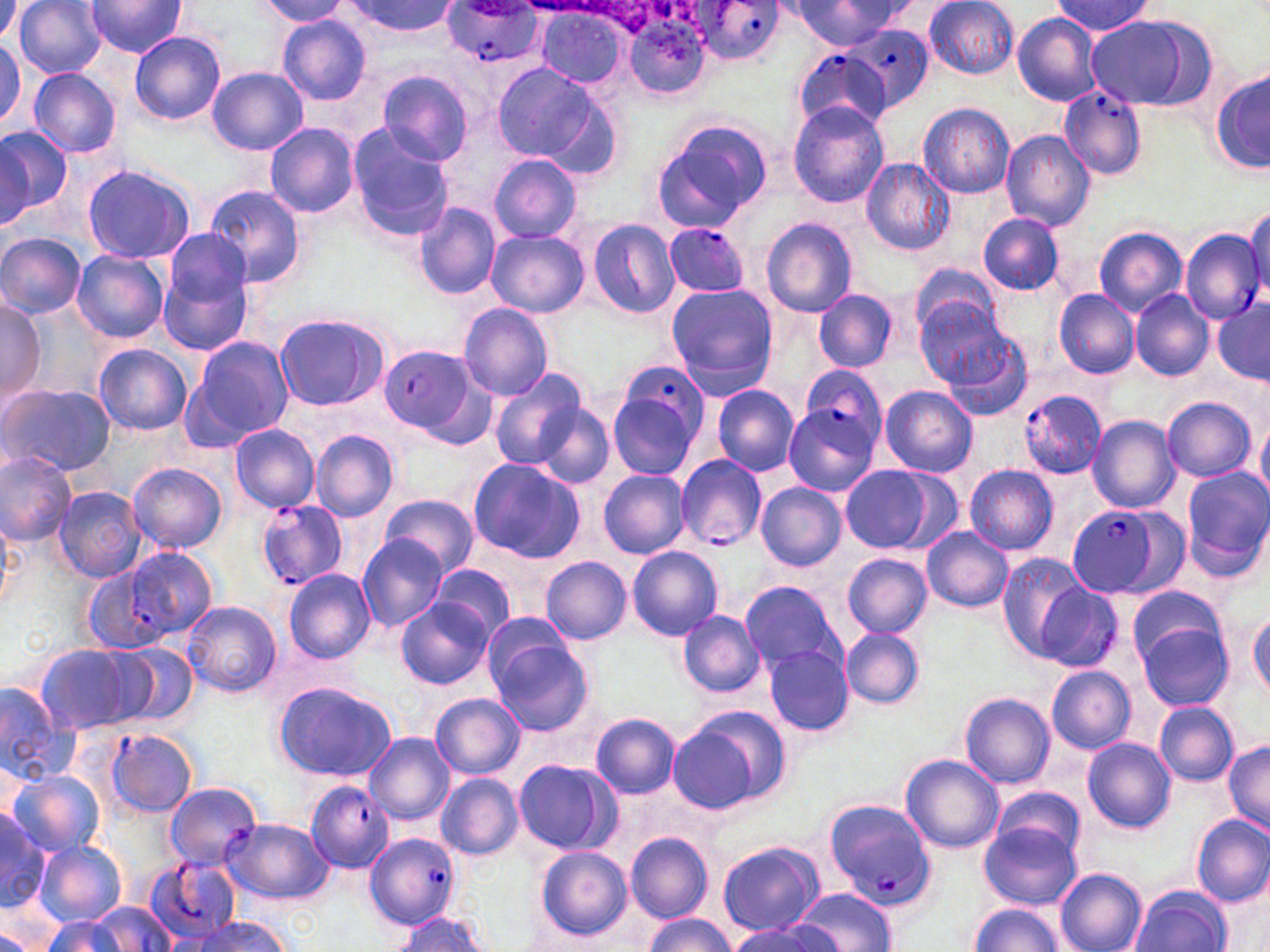
Summary:
  - Coordinate format: approximate bounding boxes as named x1/y1/x2/y2 corners in pixels
  - Plasmodium falciparum-infected red blood cell locations: (x1=694, y1=1, x2=784, y2=66), (x1=439, y1=5, x2=548, y2=68), (x1=849, y1=26, x2=935, y2=113), (x1=792, y1=51, x2=891, y2=133), (x1=1057, y1=86, x2=1148, y2=182), (x1=664, y1=223, x2=748, y2=296), (x1=1179, y1=228, x2=1265, y2=324), (x1=380, y1=345, x2=482, y2=436), (x1=803, y1=364, x2=888, y2=450), (x1=606, y1=365, x2=708, y2=480), (x1=1017, y1=388, x2=1107, y2=479), (x1=676, y1=455, x2=766, y2=549), (x1=257, y1=499, x2=348, y2=591), (x1=1068, y1=506, x2=1170, y2=598), (x1=76, y1=563, x2=169, y2=654), (x1=106, y1=728, x2=198, y2=817), (x1=301, y1=780, x2=391, y2=875), (x1=165, y1=782, x2=261, y2=869), (x1=825, y1=802, x2=938, y2=912), (x1=365, y1=833, x2=460, y2=929), (x1=144, y1=859, x2=241, y2=945)
  - Uninfected red blood cell locations: (x1=0, y1=0, x2=25, y2=40), (x1=15, y1=0, x2=107, y2=80), (x1=86, y1=0, x2=186, y2=57), (x1=924, y1=0, x2=1020, y2=79), (x1=257, y1=1, x2=351, y2=26), (x1=342, y1=1, x2=458, y2=38), (x1=789, y1=1, x2=903, y2=48), (x1=1052, y1=1, x2=1150, y2=37), (x1=535, y1=9, x2=627, y2=87), (x1=618, y1=10, x2=713, y2=101), (x1=1011, y1=13, x2=1102, y2=106), (x1=277, y1=15, x2=371, y2=105), (x1=1085, y1=15, x2=1212, y2=111), (x1=130, y1=31, x2=225, y2=125), (x1=0, y1=40, x2=25, y2=134), (x1=493, y1=63, x2=600, y2=164), (x1=207, y1=67, x2=307, y2=155), (x1=29, y1=68, x2=119, y2=158), (x1=376, y1=68, x2=475, y2=166), (x1=1214, y1=69, x2=1270, y2=173), (x1=531, y1=84, x2=624, y2=183), (x1=788, y1=101, x2=890, y2=207), (x1=917, y1=103, x2=1014, y2=199), (x1=650, y1=119, x2=771, y2=233), (x1=265, y1=123, x2=359, y2=216), (x1=0, y1=124, x2=69, y2=226), (x1=346, y1=124, x2=454, y2=238), (x1=1000, y1=130, x2=1096, y2=232), (x1=489, y1=155, x2=583, y2=243), (x1=862, y1=159, x2=955, y2=256), (x1=83, y1=164, x2=194, y2=264), (x1=202, y1=184, x2=309, y2=290), (x1=412, y1=202, x2=501, y2=299), (x1=1245, y1=207, x2=1270, y2=296), (x1=979, y1=213, x2=1064, y2=296), (x1=587, y1=218, x2=680, y2=319), (x1=761, y1=218, x2=857, y2=317), (x1=1094, y1=225, x2=1188, y2=317), (x1=166, y1=227, x2=255, y2=305), (x1=487, y1=229, x2=589, y2=319), (x1=0, y1=232, x2=86, y2=318), (x1=72, y1=250, x2=169, y2=342), (x1=157, y1=251, x2=255, y2=355), (x1=912, y1=261, x2=1004, y2=342), (x1=664, y1=283, x2=778, y2=396), (x1=1131, y1=288, x2=1212, y2=381), (x1=815, y1=289, x2=897, y2=373), (x1=1055, y1=290, x2=1140, y2=378), (x1=0, y1=296, x2=44, y2=411), (x1=916, y1=296, x2=1014, y2=387), (x1=1212, y1=299, x2=1270, y2=385), (x1=458, y1=303, x2=555, y2=399), (x1=274, y1=312, x2=386, y2=411), (x1=938, y1=331, x2=1033, y2=423), (x1=193, y1=338, x2=293, y2=442), (x1=93, y1=344, x2=191, y2=435), (x1=487, y1=368, x2=590, y2=471), (x1=0, y1=382, x2=115, y2=480), (x1=711, y1=385, x2=799, y2=477), (x1=880, y1=385, x2=978, y2=478), (x1=1163, y1=397, x2=1257, y2=482), (x1=533, y1=403, x2=615, y2=489), (x1=784, y1=406, x2=879, y2=495), (x1=1255, y1=414, x2=1270, y2=501), (x1=1087, y1=415, x2=1181, y2=512), (x1=230, y1=424, x2=320, y2=513), (x1=312, y1=430, x2=398, y2=522), (x1=0, y1=450, x2=78, y2=543), (x1=467, y1=457, x2=585, y2=563), (x1=127, y1=464, x2=227, y2=553), (x1=838, y1=464, x2=943, y2=553), (x1=964, y1=464, x2=1058, y2=555), (x1=1180, y1=467, x2=1270, y2=579), (x1=599, y1=470, x2=691, y2=558), (x1=756, y1=483, x2=846, y2=572), (x1=53, y1=486, x2=146, y2=581), (x1=380, y1=495, x2=478, y2=579), (x1=0, y1=515, x2=18, y2=608), (x1=921, y1=527, x2=1013, y2=612), (x1=357, y1=532, x2=448, y2=634), (x1=627, y1=546, x2=722, y2=640), (x1=126, y1=548, x2=217, y2=639), (x1=995, y1=552, x2=1091, y2=659), (x1=841, y1=554, x2=932, y2=638), (x1=541, y1=556, x2=632, y2=644), (x1=432, y1=565, x2=513, y2=640), (x1=283, y1=568, x2=375, y2=662), (x1=739, y1=579, x2=843, y2=671), (x1=1127, y1=585, x2=1229, y2=676), (x1=396, y1=597, x2=493, y2=690), (x1=183, y1=599, x2=280, y2=697), (x1=678, y1=611, x2=765, y2=697), (x1=1249, y1=611, x2=1270, y2=697), (x1=484, y1=615, x2=580, y2=700), (x1=1135, y1=617, x2=1233, y2=712), (x1=839, y1=627, x2=925, y2=708), (x1=488, y1=637, x2=595, y2=737), (x1=110, y1=641, x2=198, y2=729), (x1=37, y1=644, x2=143, y2=735), (x1=764, y1=644, x2=854, y2=736), (x1=1045, y1=666, x2=1136, y2=753), (x1=273, y1=681, x2=397, y2=781), (x1=0, y1=685, x2=77, y2=785), (x1=960, y1=692, x2=1056, y2=788), (x1=430, y1=693, x2=526, y2=780), (x1=1155, y1=703, x2=1238, y2=785), (x1=590, y1=713, x2=682, y2=800), (x1=668, y1=719, x2=761, y2=811), (x1=365, y1=732, x2=453, y2=825), (x1=1083, y1=737, x2=1176, y2=832), (x1=1223, y1=740, x2=1270, y2=836), (x1=900, y1=753, x2=1005, y2=854), (x1=514, y1=758, x2=615, y2=854), (x1=8, y1=770, x2=104, y2=858), (x1=437, y1=773, x2=525, y2=861), (x1=995, y1=787, x2=1085, y2=866), (x1=0, y1=812, x2=54, y2=913), (x1=1191, y1=813, x2=1270, y2=907), (x1=979, y1=820, x2=1082, y2=911), (x1=626, y1=832, x2=715, y2=924), (x1=35, y1=841, x2=126, y2=925), (x1=717, y1=841, x2=823, y2=936), (x1=534, y1=847, x2=633, y2=942), (x1=1056, y1=868, x2=1147, y2=952), (x1=1130, y1=885, x2=1232, y2=952), (x1=792, y1=888, x2=898, y2=952), (x1=90, y1=901, x2=175, y2=950), (x1=970, y1=904, x2=1065, y2=951), (x1=391, y1=912, x2=489, y2=951), (x1=42, y1=914, x2=129, y2=952), (x1=643, y1=914, x2=737, y2=951), (x1=185, y1=917, x2=293, y2=951), (x1=730, y1=921, x2=834, y2=952), (x1=0, y1=927, x2=41, y2=951)
  - Slide-level diagnosis: Plasmodium falciparum
  - Modality: light microscopy
  - Field of view: single
  - Magnification: 1000x
  - Stain: May-Grünwald-Giemsa
  - Image size: 1270×952 pixels
  - Preparation: thin blood smear